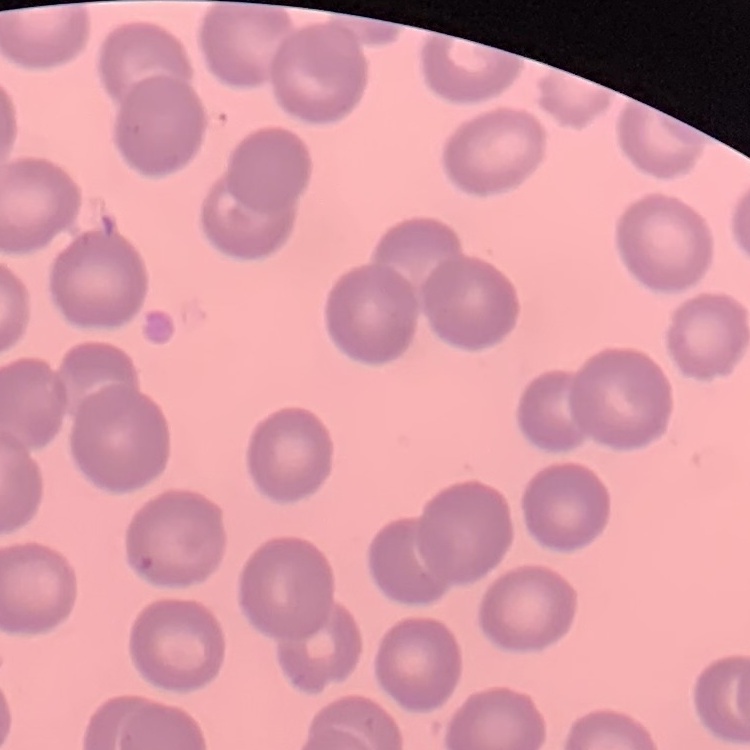
Summary:
  - Erythrocyte morphology: no rouleaux formation
  - Stain: Field's or Giemsa
  - Preparation: thin peripheral smear
  - Image type: square crop of a larger photomicrograph